Report the malaria status of this cell.
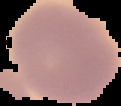

It is uninfected.

Summary:
  - Image type: cell region segmented out of the field of view; surrounding area masked to black
  - Image size: 121×106 pixels
  - Preparation: thin blood film